Point out each leukocyte.
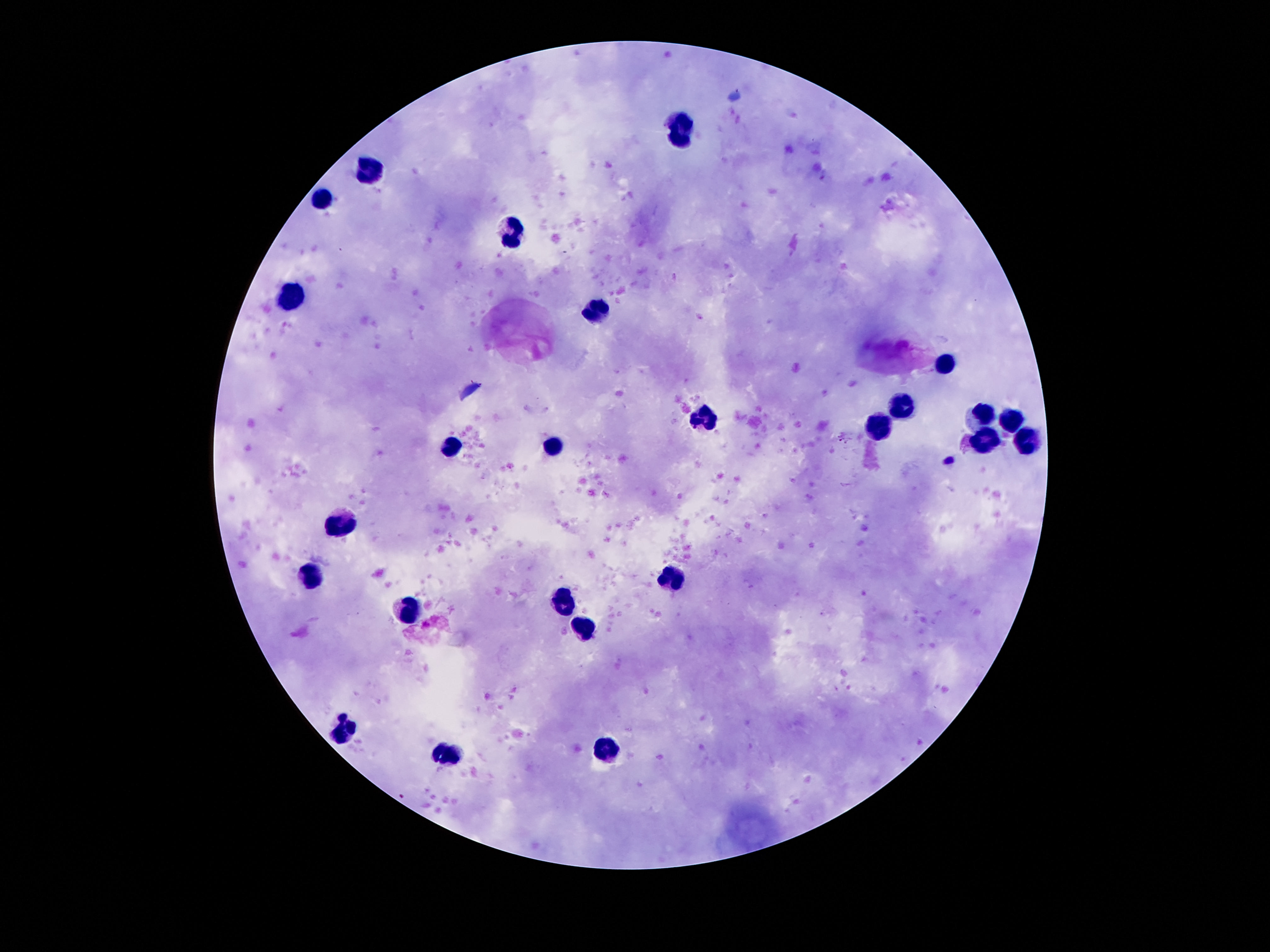
Approximate object centers, in pixels from the top-left corner.
Leukocytes: (x=680, y=130), (x=371, y=170), (x=323, y=199), (x=512, y=235), (x=294, y=299), (x=596, y=310), (x=943, y=363), (x=904, y=401), (x=983, y=419), (x=1008, y=419), (x=704, y=422), (x=882, y=423), (x=1029, y=439), (x=984, y=441), (x=448, y=446), (x=554, y=448), (x=337, y=515), (x=673, y=576), (x=312, y=578), (x=563, y=603), (x=405, y=612), (x=588, y=628), (x=343, y=730), (x=607, y=750), (x=448, y=756).

capture = smartphone camera through the microscope eyepiece
magnification = 100x
preparation = thick blood film
image size = 1270×952 pixels
field of view = one from this slide
stain = Giemsa
patient malaria status = not infected